Name the parasite shown.
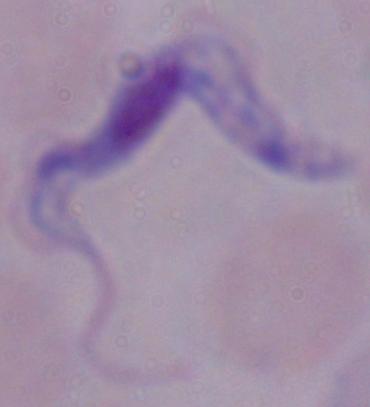
A trypanosome.

Summary:
  - Modality: photomicrograph
  - Magnification: 1000x